Name the parasite shown.
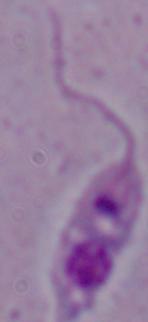
This is Leishmania.

magnification: 1000x
modality: photomicrograph